Assess the morphology of the red blood cells.
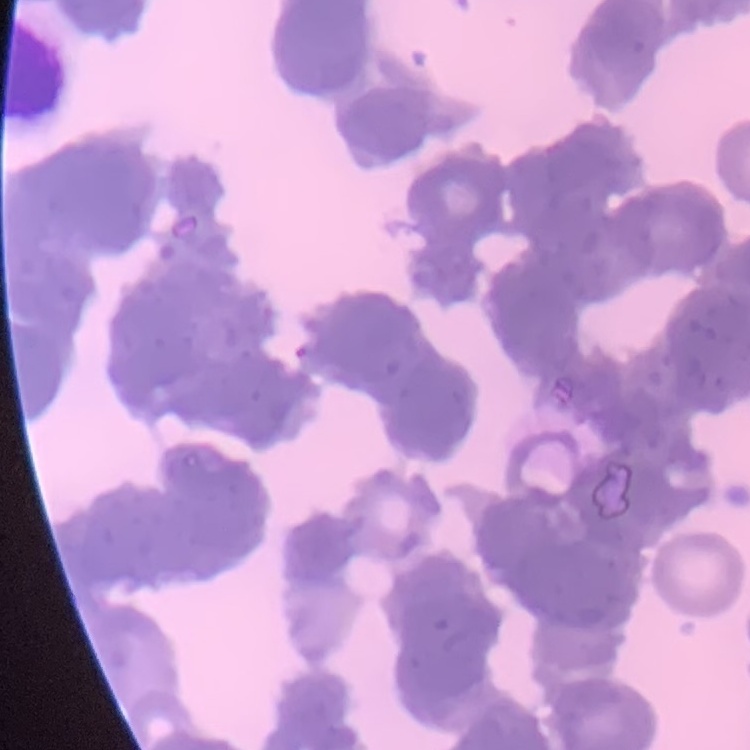

Rouleaux formation.

Thin blood smear. One tile cut from a larger photomicrograph. Stained with either Field's or Giemsa.